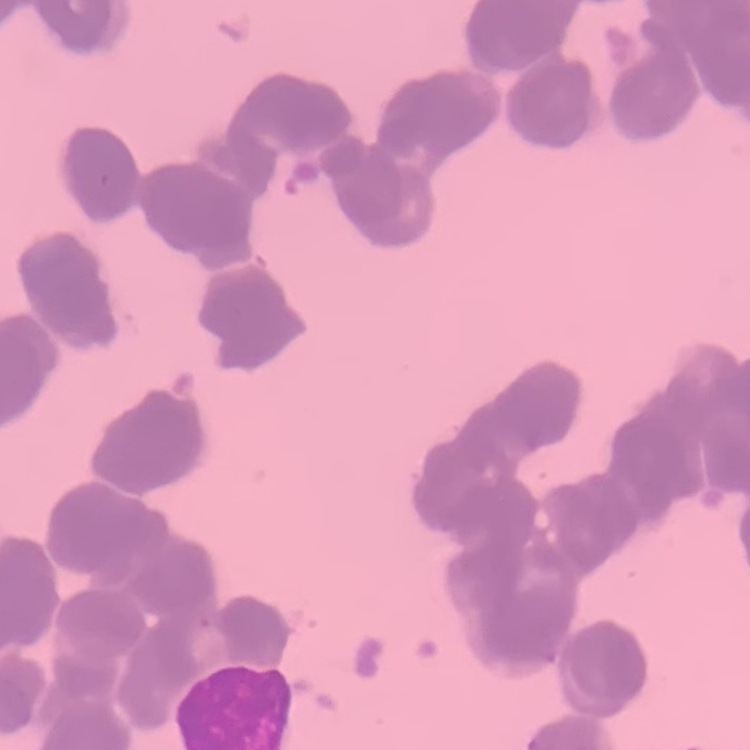 The erythrocytes show rouleaux formation. Field's or Giemsa stain. Square crop of a larger photomicrograph. Thin peripheral smear.